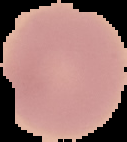
result = negative for Plasmodium parasites
image size = 127×142 pixels
preparation = thin blood film
image type = cell region segmented out of the field of view; surrounding area masked to black